Classify this cell by malaria status.
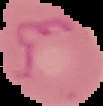
It is parasitized.

image size = 103×106 pixels
preparation = thin blood smear
image type = segmented cell region with the area outside set to black